Locate and identify every blood parasite.
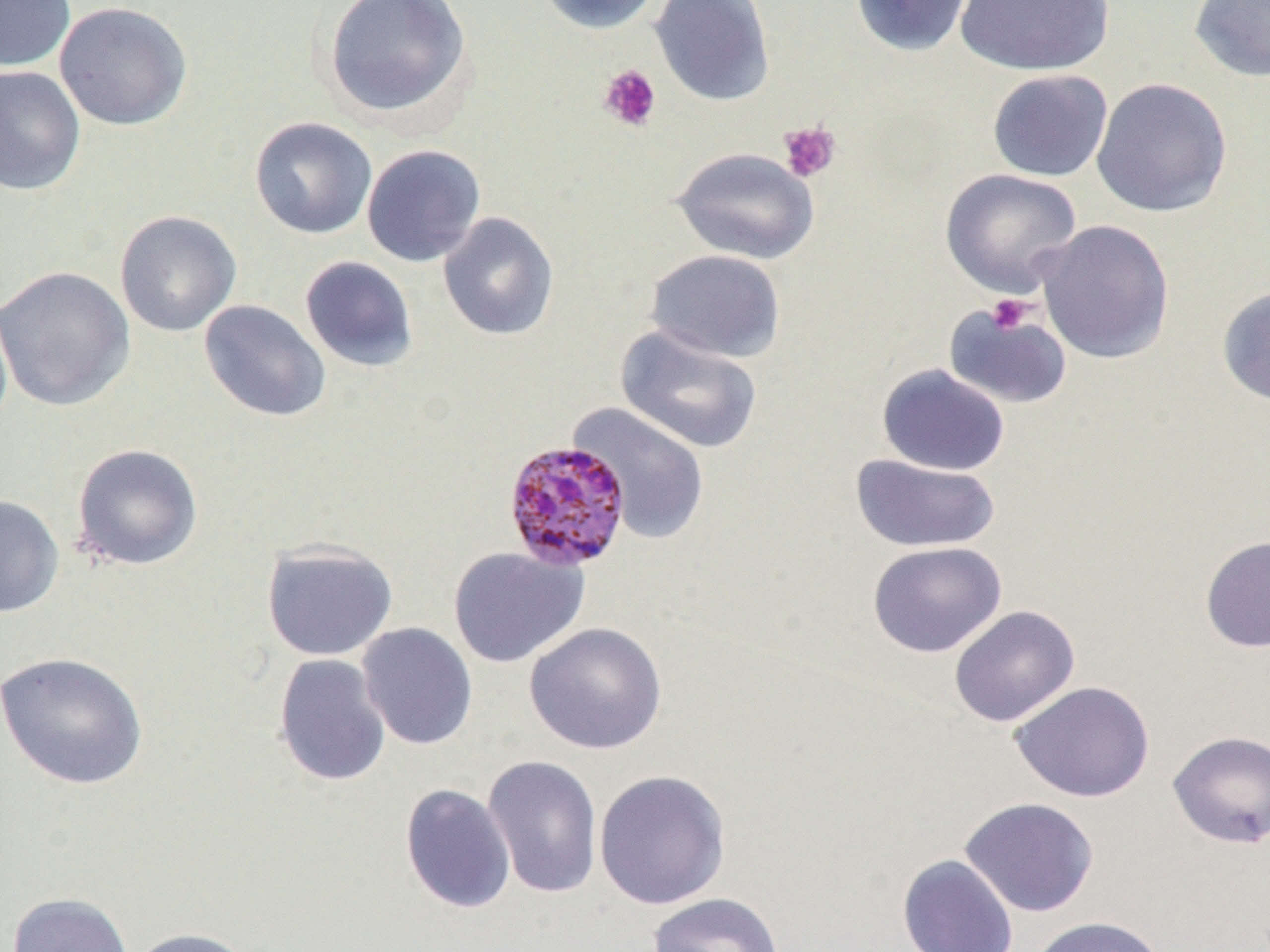
Approximate bounding boxes as named x1/y1/x2/y2 corners in pixels.
Plasmodium malariae-infected red blood cells: (x1=503, y1=439, x2=631, y2=572).
No Plasmodium falciparum, Plasmodium ovale, Plasmodium vivax, Babesia divergens, or Trypanosoma brucei observed.

slide-level diagnosis = Plasmodium malariae
uninfected red blood cell locations = approximate bounding boxes as named x1/y1/x2/y2 corners in pixels: (x1=0, y1=0, x2=76, y2=71), (x1=321, y1=0, x2=473, y2=124), (x1=535, y1=0, x2=663, y2=35), (x1=649, y1=0, x2=776, y2=106), (x1=850, y1=0, x2=976, y2=56), (x1=956, y1=0, x2=1114, y2=76), (x1=1188, y1=0, x2=1270, y2=82), (x1=54, y1=1, x2=192, y2=131), (x1=0, y1=65, x2=86, y2=196), (x1=987, y1=69, x2=1113, y2=182), (x1=1091, y1=77, x2=1233, y2=218), (x1=249, y1=116, x2=378, y2=239), (x1=361, y1=144, x2=486, y2=267), (x1=670, y1=146, x2=820, y2=265), (x1=940, y1=168, x2=1082, y2=298), (x1=114, y1=210, x2=242, y2=337), (x1=438, y1=212, x2=560, y2=341), (x1=1036, y1=219, x2=1175, y2=363), (x1=644, y1=249, x2=787, y2=363), (x1=299, y1=256, x2=419, y2=372), (x1=0, y1=265, x2=135, y2=411), (x1=1217, y1=285, x2=1270, y2=406), (x1=0, y1=299, x2=13, y2=437), (x1=198, y1=299, x2=331, y2=423), (x1=943, y1=301, x2=1072, y2=409), (x1=614, y1=325, x2=764, y2=455), (x1=876, y1=364, x2=1010, y2=476), (x1=568, y1=402, x2=711, y2=543), (x1=71, y1=443, x2=204, y2=572), (x1=850, y1=452, x2=1001, y2=552), (x1=0, y1=494, x2=65, y2=618), (x1=1200, y1=535, x2=1270, y2=653), (x1=260, y1=539, x2=398, y2=661), (x1=867, y1=541, x2=1007, y2=658), (x1=448, y1=545, x2=589, y2=668), (x1=948, y1=605, x2=1080, y2=727), (x1=524, y1=621, x2=667, y2=755), (x1=356, y1=622, x2=478, y2=750), (x1=0, y1=651, x2=150, y2=791), (x1=272, y1=653, x2=392, y2=787), (x1=1010, y1=681, x2=1155, y2=803), (x1=1167, y1=730, x2=1270, y2=849), (x1=482, y1=754, x2=603, y2=899), (x1=593, y1=769, x2=731, y2=910), (x1=399, y1=783, x2=517, y2=914), (x1=959, y1=797, x2=1099, y2=917), (x1=897, y1=853, x2=1019, y2=952), (x1=6, y1=892, x2=134, y2=952), (x1=646, y1=892, x2=784, y2=952), (x1=1029, y1=915, x2=1169, y2=952), (x1=125, y1=926, x2=256, y2=952)
modality = light microscopy
magnification = 1000x
preparation = thin blood smear
platelet locations = approximate bounding boxes as named x1/y1/x2/y2 corners in pixels: (x1=598, y1=63, x2=661, y2=132), (x1=778, y1=121, x2=841, y2=182), (x1=986, y1=294, x2=1034, y2=335)
field of view = one of a larger specimen
image size = 1270×952 pixels